Name the parasite shown.
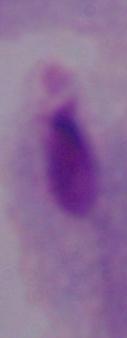
A trichomonad.

Summary:
  - Modality: photomicrograph
  - Magnification: 1000x